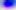

Summary:
  - Magnification: 400x
  - Modality: micrograph
  - Identification: Toxoplasma gondii